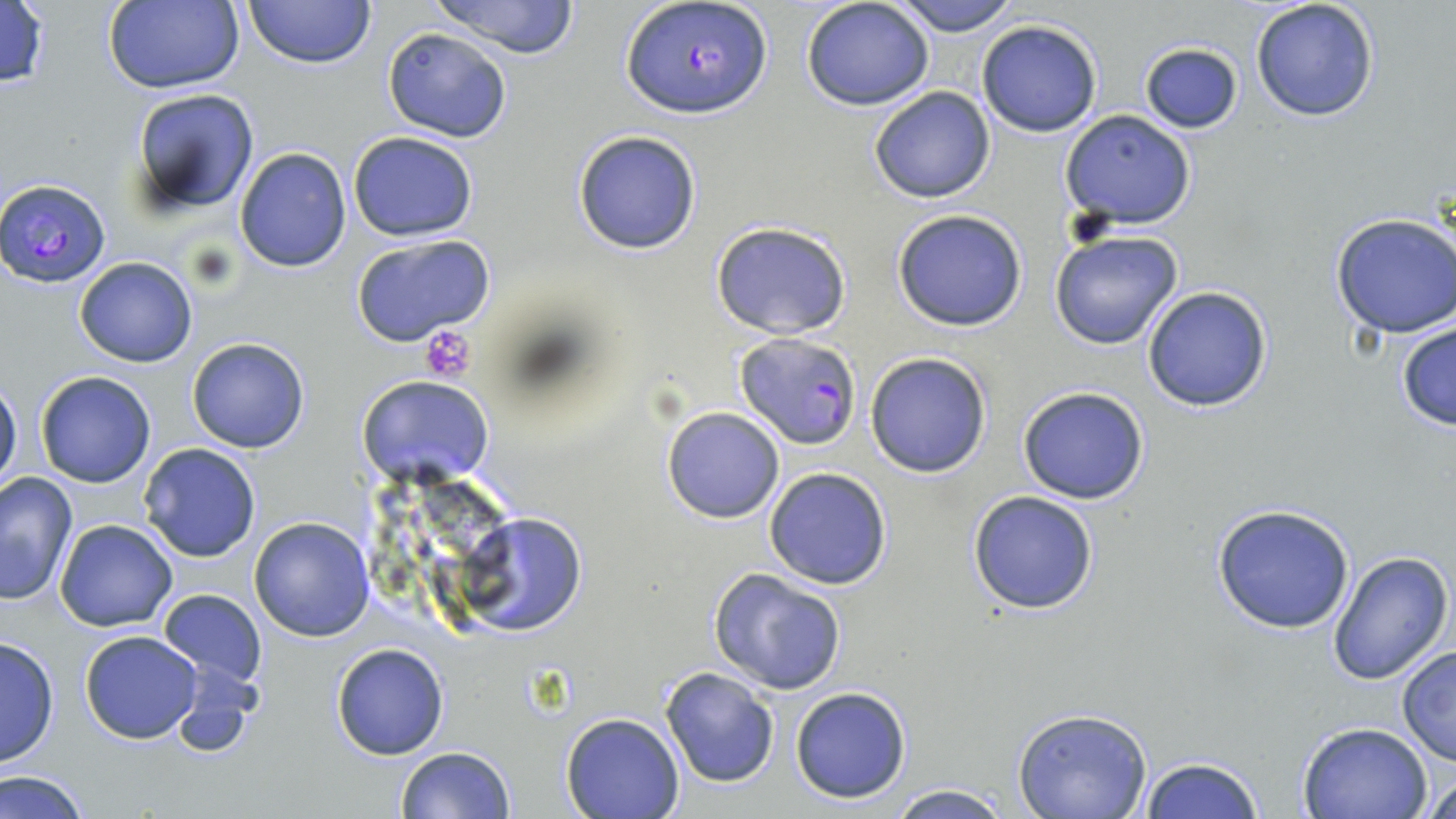

Summary:
  - Coordinate format: approximate bounding boxes as [x1, y1, x2, y2] in pixels
  - Platelet locations: [420, 323, 477, 383]
  - Plasmodium falciparum-infected red blood cell locations: [622, 1, 772, 120], [3, 176, 111, 289], [734, 333, 861, 449]
  - Uninfected red blood cell locations: [0, 0, 52, 92], [244, 0, 373, 68], [891, 0, 1017, 37], [1250, 0, 1380, 123], [102, 1, 244, 93], [427, 1, 582, 60], [801, 1, 936, 111], [976, 19, 1103, 137], [381, 27, 513, 143], [1138, 40, 1243, 134], [868, 85, 997, 203], [127, 89, 258, 218], [1059, 110, 1197, 231], [571, 129, 702, 255], [348, 132, 478, 241], [233, 147, 352, 273], [892, 208, 1028, 332], [1330, 212, 1456, 338], [711, 220, 852, 340], [1049, 231, 1184, 350], [349, 235, 495, 348], [74, 257, 198, 369], [1141, 284, 1274, 413], [1394, 321, 1456, 432], [186, 337, 311, 453], [864, 351, 992, 477], [34, 371, 158, 488], [357, 375, 494, 488], [0, 380, 22, 492], [1017, 385, 1149, 504], [661, 406, 785, 524], [138, 442, 262, 563], [763, 467, 894, 590], [0, 472, 77, 607], [965, 490, 1100, 615], [1210, 502, 1356, 634], [455, 511, 586, 637], [249, 516, 377, 641], [55, 519, 178, 631], [1328, 550, 1455, 688], [708, 567, 847, 695], [156, 588, 268, 689], [80, 630, 203, 744], [0, 635, 60, 770], [331, 642, 450, 761], [1396, 646, 1456, 765], [659, 667, 779, 788], [165, 669, 259, 763], [789, 685, 913, 804], [1012, 709, 1155, 819], [559, 713, 686, 819], [1298, 721, 1433, 818], [394, 746, 516, 819], [1137, 757, 1265, 819], [1423, 767, 1455, 819], [1, 769, 93, 819], [882, 784, 1018, 819]
  - Slide-level diagnosis: Plasmodium falciparum
  - Preparation: thin blood smear
  - Modality: light microscopy
  - Image size: 1456×819 pixels
  - Stain: May-Grünwald-Giemsa
  - Magnification: 1000x
  - Field of view: one of a larger specimen